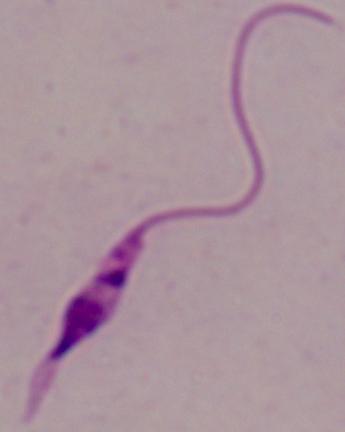
{
  "identification": "Leishmania",
  "modality": "micrograph",
  "magnification": "1000x"
}